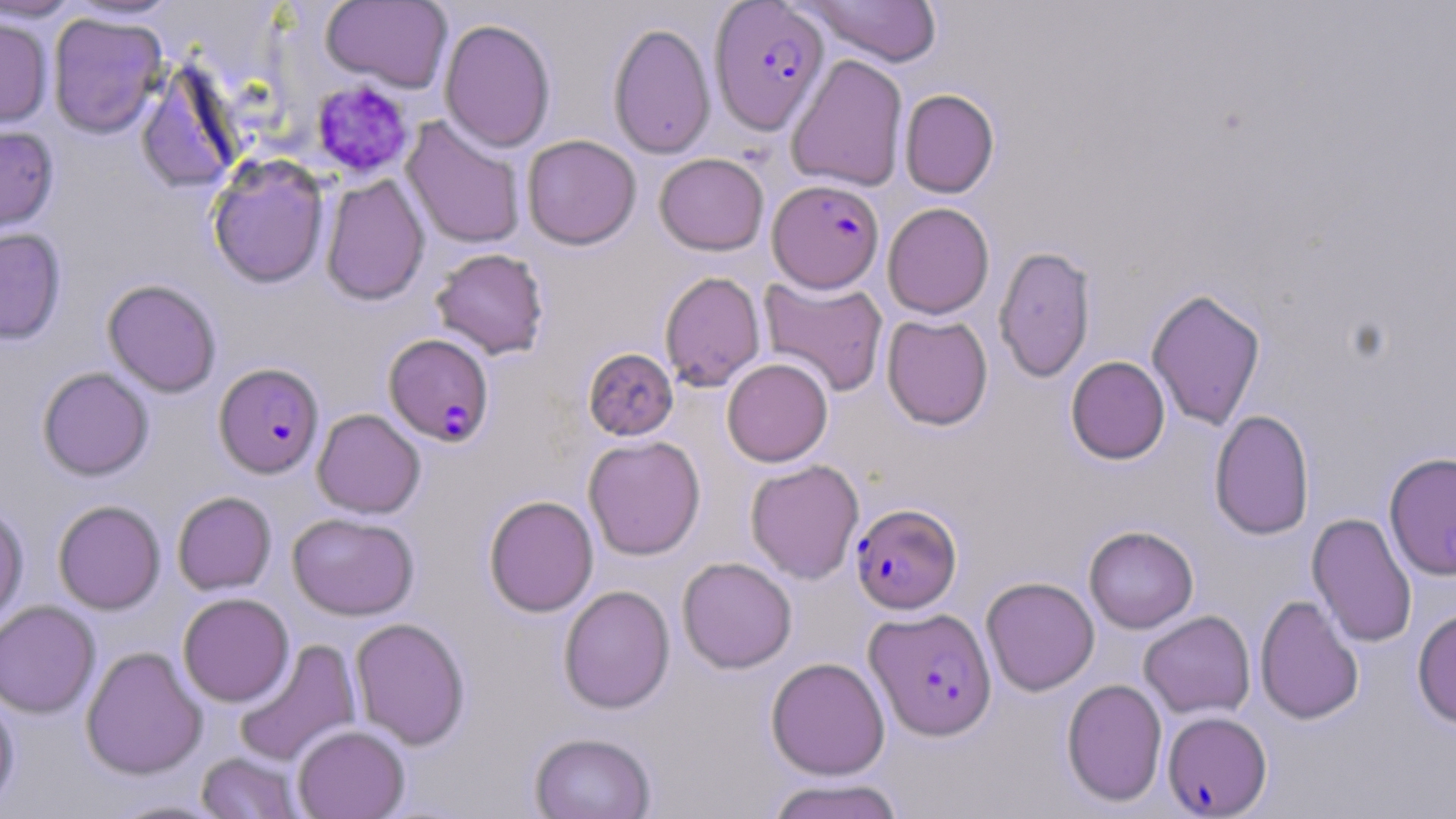
Summary:
  - Coordinate format: approximate bounding boxes as [x1, y1, x2, y2] in pixels
  - Plasmodium falciparum-infected red blood cell locations: [709, 1, 830, 135], [768, 179, 884, 292], [384, 334, 495, 447], [214, 363, 324, 478], [851, 503, 961, 614], [865, 607, 997, 740], [1162, 711, 1272, 816]
  - Platelet locations: [310, 80, 415, 179]
  - Uninfected red blood cell locations: [0, 0, 84, 22], [799, 0, 943, 67], [321, 1, 453, 92], [47, 12, 167, 138], [0, 15, 53, 130], [439, 18, 556, 152], [608, 21, 716, 159], [786, 54, 908, 192], [135, 63, 244, 194], [899, 88, 999, 198], [401, 117, 526, 249], [0, 125, 59, 234], [522, 134, 641, 250], [654, 153, 769, 255], [207, 154, 330, 288], [320, 173, 430, 306], [883, 202, 995, 319], [0, 227, 66, 345], [993, 245, 1096, 383], [430, 247, 549, 359], [659, 271, 765, 392], [758, 275, 889, 397], [102, 279, 221, 397], [1147, 287, 1266, 431], [881, 314, 993, 430], [583, 348, 678, 441], [1065, 356, 1170, 464], [721, 358, 833, 466], [37, 367, 154, 480], [312, 409, 425, 518], [1209, 409, 1314, 541], [583, 435, 706, 560], [1383, 451, 1456, 581], [746, 459, 864, 584], [172, 491, 276, 595], [484, 495, 599, 617], [53, 499, 165, 614], [0, 505, 28, 627], [1307, 512, 1418, 648], [288, 513, 419, 620], [1084, 525, 1199, 633], [677, 557, 797, 673], [981, 576, 1100, 696], [558, 585, 675, 714], [178, 592, 294, 707], [1255, 594, 1364, 725], [0, 601, 100, 719], [1412, 607, 1456, 730], [1139, 611, 1256, 719], [350, 618, 470, 750], [232, 639, 362, 767], [81, 646, 207, 780], [766, 657, 890, 780], [1061, 678, 1167, 807], [0, 691, 20, 811], [292, 724, 410, 819], [528, 732, 656, 818], [196, 752, 303, 819], [764, 777, 908, 819], [101, 797, 234, 818]
  - Slide-level diagnosis: Plasmodium falciparum
  - Field of view: one of a larger specimen
  - Stain: May-Grünwald-Giemsa
  - Preparation: thin blood film
  - Magnification: 1000x
  - Image size: 1456×819 pixels
  - Modality: optical microscopy